Name the cell type shown.
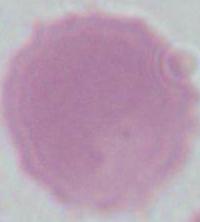

An erythrocyte.

{
  "modality": "micrograph",
  "magnification": "1000x"
}